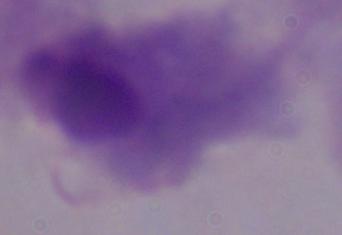

Summary:
  - Identification: trichomonad
  - Modality: photomicrograph
  - Magnification: 1000x